Point out every Plasmodium parasite and every leukocyte.
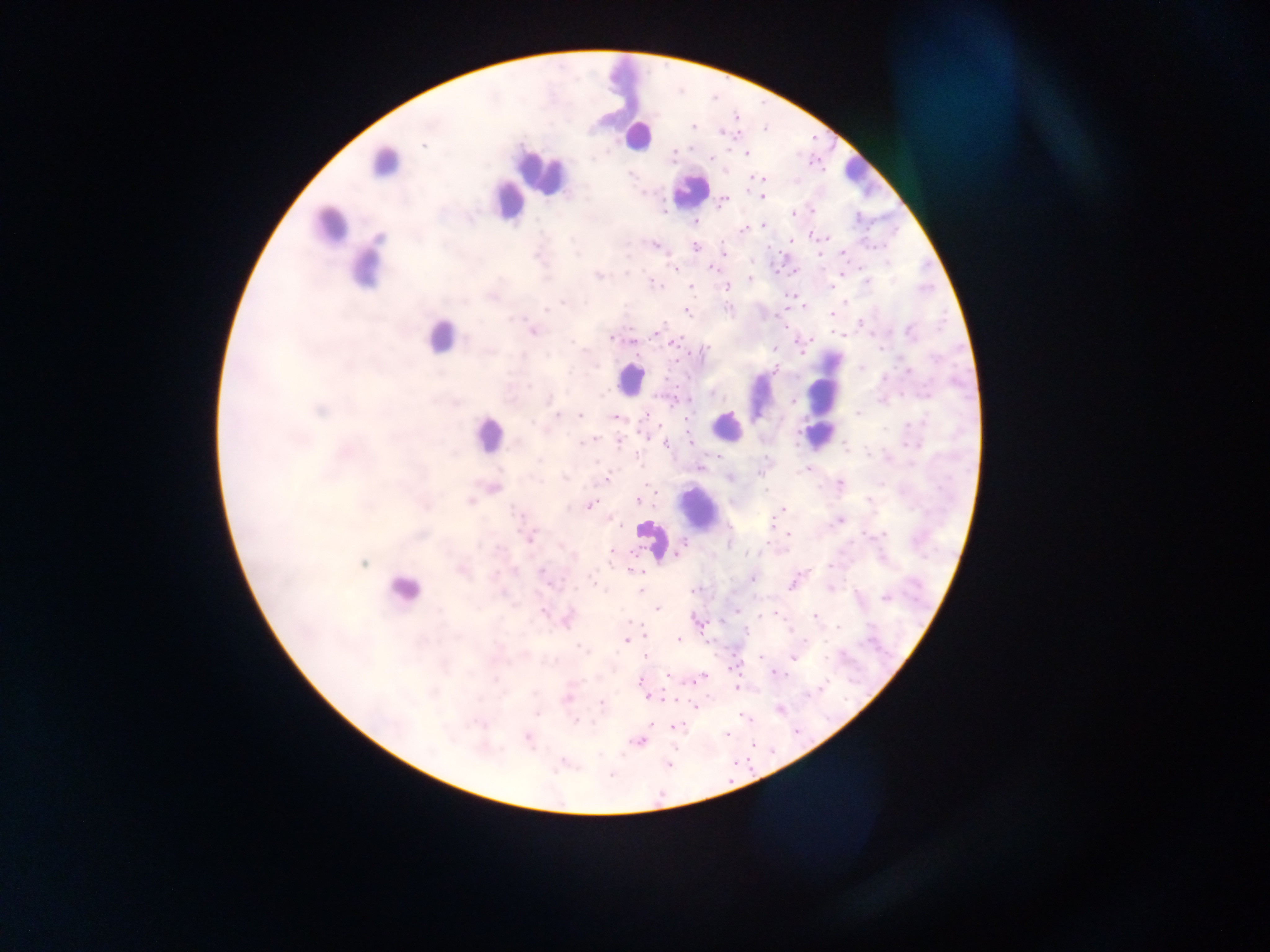
Approximate centers as {x, y} in pixels.
Plasmodium parasites: {432, 120}, {430, 126}, {764, 126}, {694, 127}, {723, 133}, {426, 143}, {675, 152}, {745, 154}, {710, 156}, {631, 174}, {755, 177}, {750, 178}, {765, 178}, {763, 197}, {721, 203}, {795, 215}, {859, 219}, {695, 224}, {764, 226}, {743, 229}, {809, 235}, {827, 239}, {791, 242}, {656, 245}, {695, 247}, {725, 251}, {844, 254}, {674, 267}, {712, 268}, {626, 272}, {843, 275}, {599, 276}, {750, 279}, {867, 282}, {653, 283}, {725, 287}, {690, 288}, {795, 300}, {845, 302}, {563, 303}, {546, 309}, {729, 309}, {687, 311}, {834, 313}, {516, 319}, {862, 322}, {785, 327}, {533, 331}, {839, 333}, {612, 337}, {632, 341}, {796, 341}, {675, 343}, {491, 350}, {585, 351}, {862, 368}, {908, 371}, {572, 372}, {528, 383}, {549, 399}, {668, 400}, {860, 414}, {644, 416}, {561, 417}, {580, 417}, {614, 418}, {686, 418}, {644, 434}, {590, 440}, {690, 441}, {580, 443}, {666, 444}, {619, 445}, {845, 449}, {700, 466}, {807, 469}, {605, 479}, {638, 500}, {591, 504}, {783, 510}, {536, 534}, {790, 535}, {529, 538}, {681, 546}, {612, 553}, {637, 556}, {830, 567}, {542, 569}, {632, 570}, {493, 576}, {592, 577}, {754, 578}, {831, 589}, {639, 590}, {692, 592}, {884, 598}, {655, 607}, {543, 612}, {775, 613}, {761, 614}, {814, 617}, {695, 618}, {700, 621}, {628, 622}, {566, 623}, {641, 624}, {838, 628}, {791, 633}, {457, 637}, {677, 640}, {627, 641}, {708, 643}, {582, 647}, {647, 654}, {792, 658}, {733, 666}, {670, 675}, {775, 675}, {494, 677}, {703, 678}, {638, 680}, {736, 689}, {534, 693}, {645, 696}, {566, 698}, {660, 698}, {677, 700}, {601, 704}, {695, 706}, {779, 710}, {743, 717}, {575, 722}, {673, 727}, {724, 735}, {527, 738}, {639, 741}, {754, 746}, {746, 759}, {670, 766}, {611, 774}, {731, 780}.
Leukocytes: {638, 139}, {391, 168}, {854, 169}, {690, 192}, {511, 205}, {333, 221}, {364, 274}, {438, 339}, {624, 375}, {819, 408}, {731, 421}, {484, 452}, {693, 513}, {400, 590}.

preparation = thick blood smear
field of view = single
capture = mobile-phone photograph through a microscope
country = Ghana
image size = 1270×952 pixels